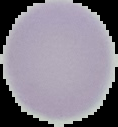

Summary:
  - Image type: segmented cell region with the area outside set to black
  - Preparation: thin blood film
  - Malaria status: uninfected
  - Image size: 118×127 pixels